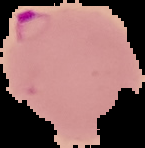
malaria_status: parasitized
image_size: 145×148 pixels
preparation: thin blood film
image_type: cell region segmented out of the field of view; surrounding area masked to black